Mark where platelets are.
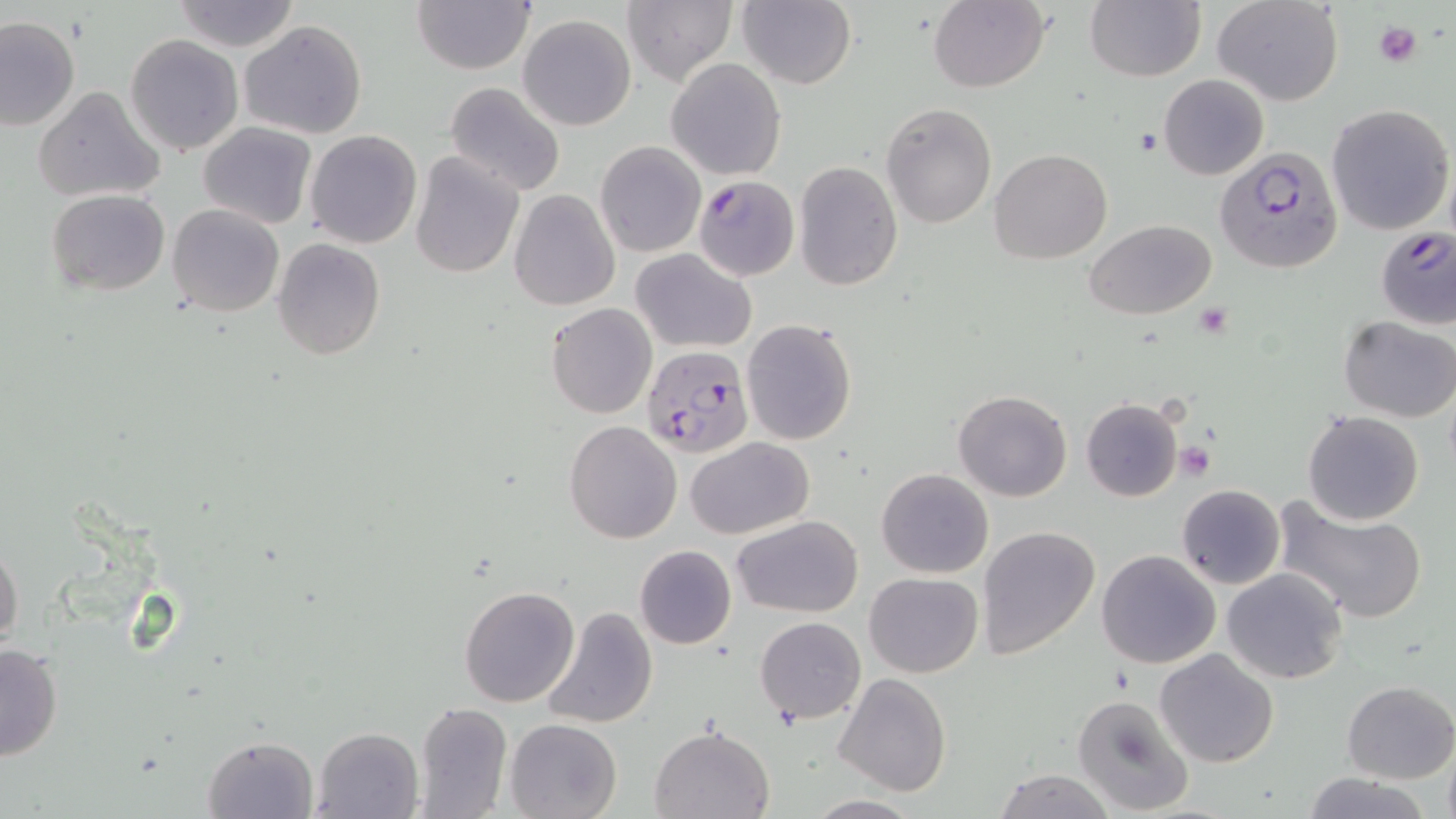

Approximate bounding boxes as named x1/y1/x2/y2 corners in pixels.
Platelets: (x1=1374, y1=18, x2=1423, y2=68), (x1=1175, y1=441, x2=1216, y2=479).

slide_level_diagnosis: Plasmodium falciparum
field_of_view: one of a larger specimen
preparation: thin blood film
uninfected_red_blood_cell_locations: 'approximate bounding boxes as named x1/y1/x2/y2 corners in pixels: (x1=170, y1=0, x2=301, y2=51), (x1=736, y1=0, x2=856, y2=89), (x1=929, y1=0, x2=1050, y2=92), (x1=1214, y1=0, x2=1344, y2=106), (x1=411, y1=1, x2=536, y2=73), (x1=622, y1=2, x2=737, y2=87), (x1=1084, y1=2, x2=1205, y2=82), (x1=517, y1=14, x2=637, y2=131), (x1=0, y1=17, x2=78, y2=131), (x1=238, y1=20, x2=368, y2=138), (x1=124, y1=34, x2=244, y2=157), (x1=665, y1=58, x2=787, y2=180), (x1=1160, y1=74, x2=1268, y2=179), (x1=444, y1=82, x2=566, y2=196), (x1=33, y1=87, x2=167, y2=204), (x1=881, y1=103, x2=996, y2=227), (x1=1325, y1=104, x2=1454, y2=234), (x1=199, y1=122, x2=317, y2=229), (x1=304, y1=129, x2=423, y2=249), (x1=595, y1=142, x2=705, y2=257), (x1=989, y1=148, x2=1112, y2=263), (x1=410, y1=152, x2=523, y2=278), (x1=793, y1=161, x2=902, y2=289), (x1=46, y1=188, x2=171, y2=296), (x1=508, y1=189, x2=621, y2=311), (x1=168, y1=203, x2=285, y2=317), (x1=1085, y1=217, x2=1216, y2=319), (x1=271, y1=237, x2=386, y2=361), (x1=632, y1=248, x2=758, y2=353), (x1=546, y1=302, x2=658, y2=419), (x1=1340, y1=317, x2=1456, y2=422), (x1=741, y1=318, x2=857, y2=446), (x1=952, y1=388, x2=1072, y2=501), (x1=1081, y1=397, x2=1183, y2=502), (x1=1302, y1=411, x2=1424, y2=526), (x1=563, y1=420, x2=682, y2=543), (x1=686, y1=436, x2=814, y2=537), (x1=877, y1=468, x2=994, y2=578), (x1=1176, y1=484, x2=1285, y2=589), (x1=1272, y1=498, x2=1429, y2=625), (x1=732, y1=515, x2=862, y2=618), (x1=977, y1=526, x2=1100, y2=658), (x1=0, y1=543, x2=24, y2=655), (x1=634, y1=544, x2=737, y2=649), (x1=1096, y1=549, x2=1221, y2=668), (x1=1221, y1=567, x2=1348, y2=684), (x1=863, y1=572, x2=983, y2=677), (x1=459, y1=584, x2=580, y2=707), (x1=541, y1=606, x2=657, y2=728), (x1=756, y1=616, x2=866, y2=724), (x1=0, y1=643, x2=62, y2=761), (x1=1156, y1=648, x2=1278, y2=767), (x1=833, y1=672, x2=951, y2=796), (x1=1340, y1=680, x2=1455, y2=783), (x1=1071, y1=693, x2=1196, y2=818), (x1=414, y1=701, x2=513, y2=819), (x1=505, y1=718, x2=621, y2=819), (x1=649, y1=725, x2=773, y2=819), (x1=313, y1=726, x2=426, y2=819), (x1=201, y1=734, x2=319, y2=818), (x1=994, y1=769, x2=1116, y2=819), (x1=1301, y1=772, x2=1434, y2=819), (x1=806, y1=797, x2=924, y2=818)'
image_size: 1456×819 pixels
plasmodium_falciparum_infected_red_blood_cell_locations: 'approximate bounding boxes as named x1/y1/x2/y2 corners in pixels: (x1=1215, y1=147, x2=1346, y2=275), (x1=691, y1=174, x2=801, y2=279), (x1=1375, y1=225, x2=1456, y2=330), (x1=642, y1=344, x2=752, y2=460)'
modality: light microscopy
magnification: 1000x
stain: May-Grünwald-Giemsa